Outline each blood parasite and name the species.
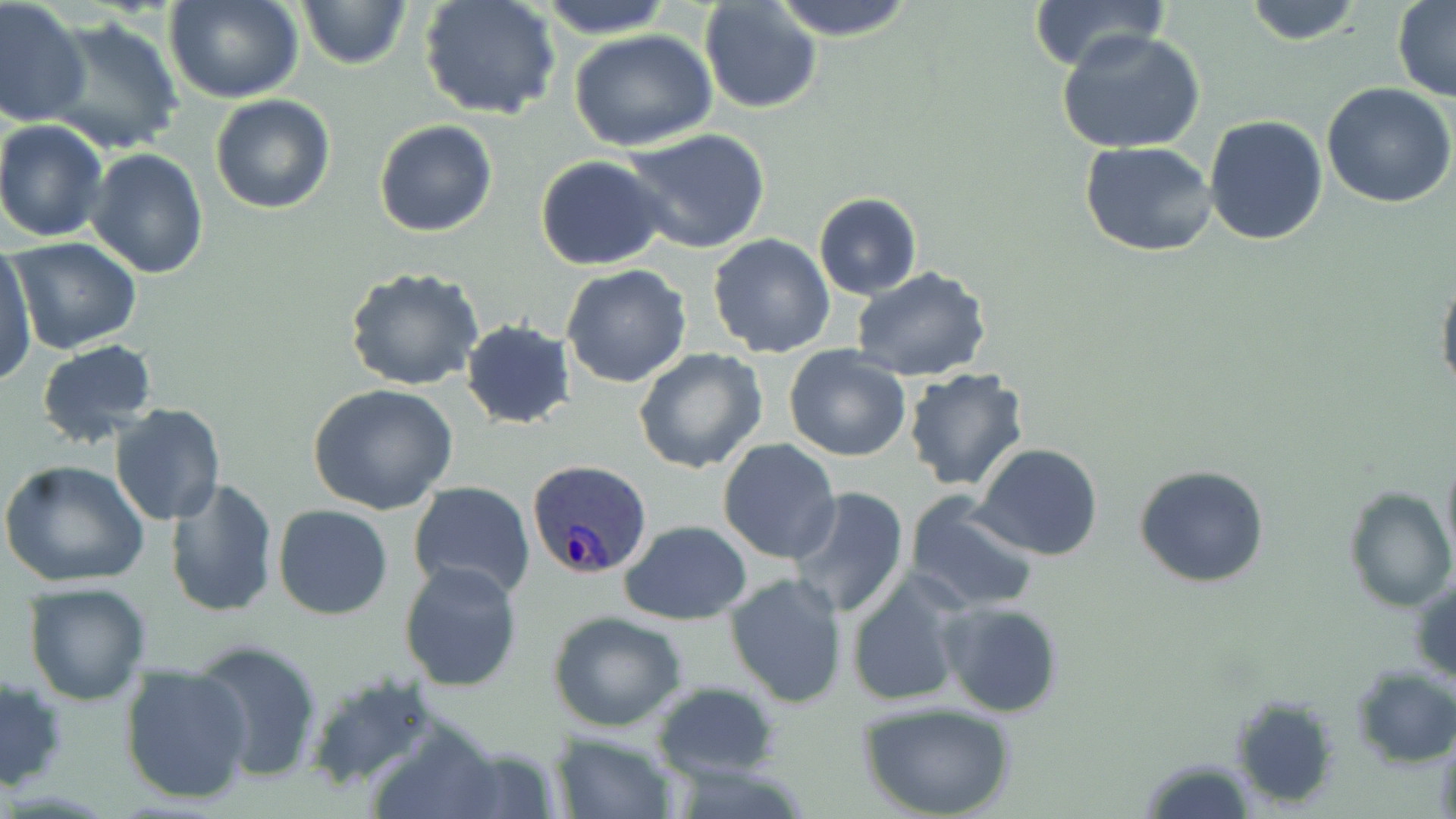

Approximate bounding boxes as named x1/y1/x2/y2 corners in pixels.
Plasmodium ovale-infected red blood cells: (x1=527, y1=459, x2=653, y2=580).
No Plasmodium falciparum, Plasmodium malariae, Plasmodium vivax, Babesia divergens, or Trypanosoma brucei observed.

Summary:
  - Uninfected red blood cell locations: (x1=0, y1=0, x2=91, y2=127), (x1=419, y1=0, x2=563, y2=123), (x1=534, y1=0, x2=676, y2=37), (x1=766, y1=0, x2=919, y2=41), (x1=1026, y1=0, x2=1175, y2=74), (x1=296, y1=1, x2=413, y2=71), (x1=698, y1=1, x2=823, y2=114), (x1=1240, y1=1, x2=1368, y2=47), (x1=1393, y1=1, x2=1455, y2=103), (x1=167, y1=2, x2=304, y2=104), (x1=45, y1=15, x2=183, y2=155), (x1=1056, y1=29, x2=1208, y2=155), (x1=569, y1=30, x2=718, y2=152), (x1=1322, y1=82, x2=1456, y2=208), (x1=209, y1=94, x2=336, y2=215), (x1=1203, y1=114, x2=1328, y2=246), (x1=0, y1=119, x2=109, y2=242), (x1=373, y1=119, x2=498, y2=237), (x1=618, y1=127, x2=772, y2=254), (x1=1080, y1=141, x2=1219, y2=257), (x1=89, y1=147, x2=208, y2=280), (x1=534, y1=154, x2=672, y2=271), (x1=812, y1=192, x2=923, y2=299), (x1=709, y1=234, x2=836, y2=357), (x1=7, y1=235, x2=142, y2=354), (x1=1, y1=241, x2=38, y2=387), (x1=560, y1=264, x2=693, y2=389), (x1=850, y1=266, x2=993, y2=383), (x1=345, y1=267, x2=484, y2=391), (x1=1437, y1=269, x2=1456, y2=401), (x1=461, y1=320, x2=578, y2=430), (x1=36, y1=339, x2=158, y2=446), (x1=783, y1=345, x2=913, y2=461), (x1=631, y1=347, x2=770, y2=475), (x1=903, y1=366, x2=1030, y2=492), (x1=307, y1=382, x2=459, y2=515), (x1=110, y1=403, x2=227, y2=527), (x1=718, y1=439, x2=841, y2=563), (x1=974, y1=443, x2=1103, y2=561), (x1=1440, y1=447, x2=1456, y2=567), (x1=0, y1=458, x2=151, y2=589), (x1=1133, y1=464, x2=1271, y2=589), (x1=165, y1=478, x2=279, y2=616), (x1=408, y1=481, x2=535, y2=602), (x1=1342, y1=485, x2=1454, y2=613), (x1=787, y1=487, x2=910, y2=620), (x1=905, y1=491, x2=1041, y2=613), (x1=273, y1=504, x2=395, y2=620), (x1=619, y1=519, x2=752, y2=626), (x1=399, y1=561, x2=523, y2=692), (x1=845, y1=571, x2=971, y2=709), (x1=1409, y1=571, x2=1456, y2=687), (x1=724, y1=575, x2=849, y2=708), (x1=23, y1=581, x2=152, y2=706), (x1=939, y1=601, x2=1064, y2=718), (x1=548, y1=610, x2=692, y2=733), (x1=191, y1=640, x2=324, y2=784), (x1=119, y1=664, x2=255, y2=805), (x1=1350, y1=666, x2=1456, y2=770), (x1=0, y1=674, x2=68, y2=790), (x1=299, y1=674, x2=447, y2=792), (x1=650, y1=681, x2=781, y2=783), (x1=1231, y1=695, x2=1341, y2=809), (x1=861, y1=703, x2=1015, y2=819), (x1=549, y1=731, x2=677, y2=819), (x1=1138, y1=756, x2=1257, y2=817)
  - Slide-level diagnosis: Plasmodium ovale
  - Field of view: one of a larger specimen
  - Modality: optical microscopy
  - Image size: 1456×819 pixels
  - Preparation: thin blood smear
  - Magnification: 1000x
  - Stain: May-Grünwald-Giemsa